Evaluate for parasitized red blood cells.
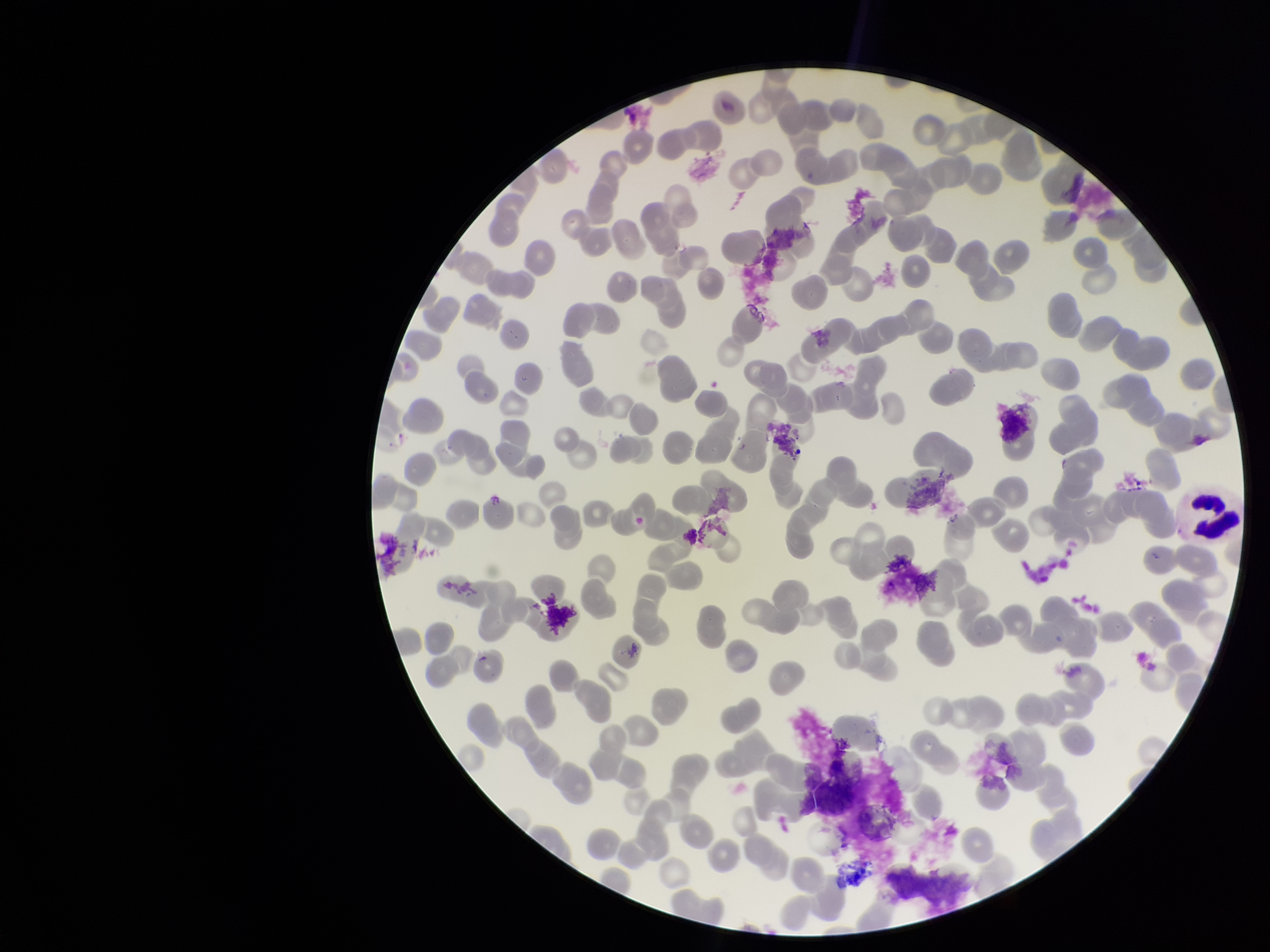
None seen.

Single field of view. Parasitized red blood cell count: 0. Preparation: thin. Photographed through the microscope eyepiece with a smartphone camera. Stained with Giemsa. Red blood cell count: 249. Image is 1270×952 pixels. Patient malaria status: negative.